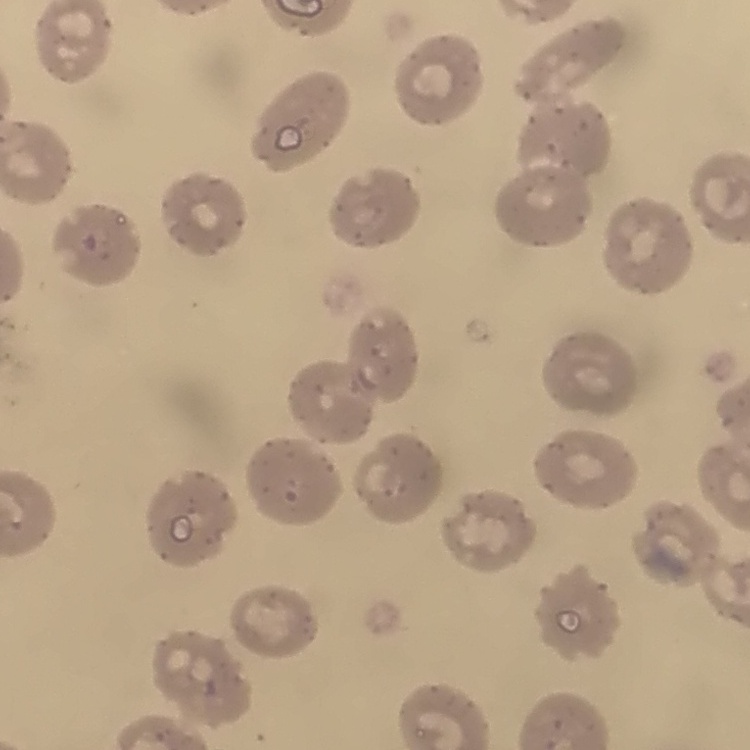
The red blood cells exhibit no rouleaux formation. Thin blood film. Field's or Giemsa stain. One tile cut from a larger photomicrograph.